Describe the morphology of the red blood cells.
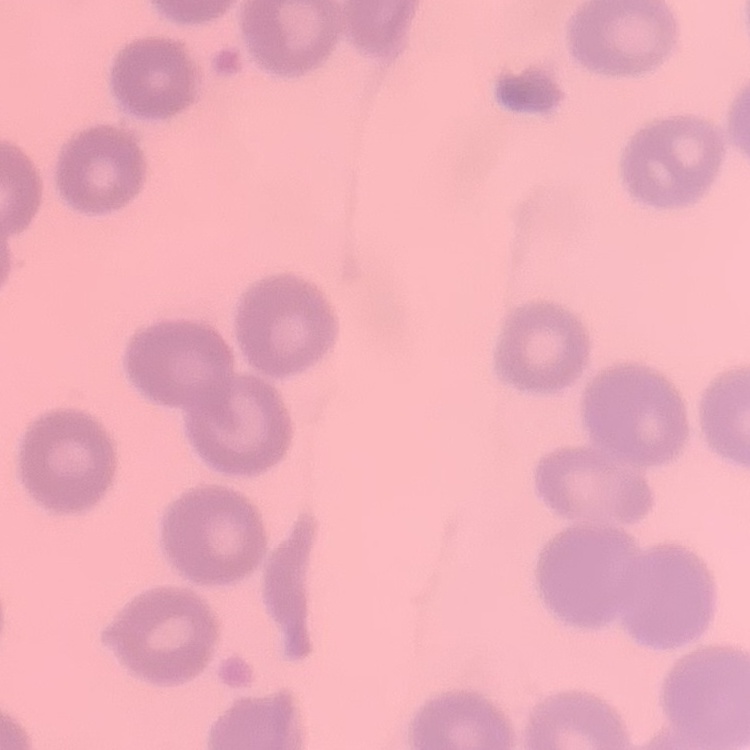
No rouleaux formation.

Summary:
  - Preparation: thin peripheral smear
  - Stain: Field's or Giemsa
  - Image type: one tile cut from a larger photomicrograph